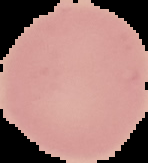
Summary:
  - Result: no Plasmodium parasites detected
  - Image size: 148×163 pixels
  - Preparation: thin blood smear
  - Image type: cell region segmented out of the field of view; surrounding area masked to black